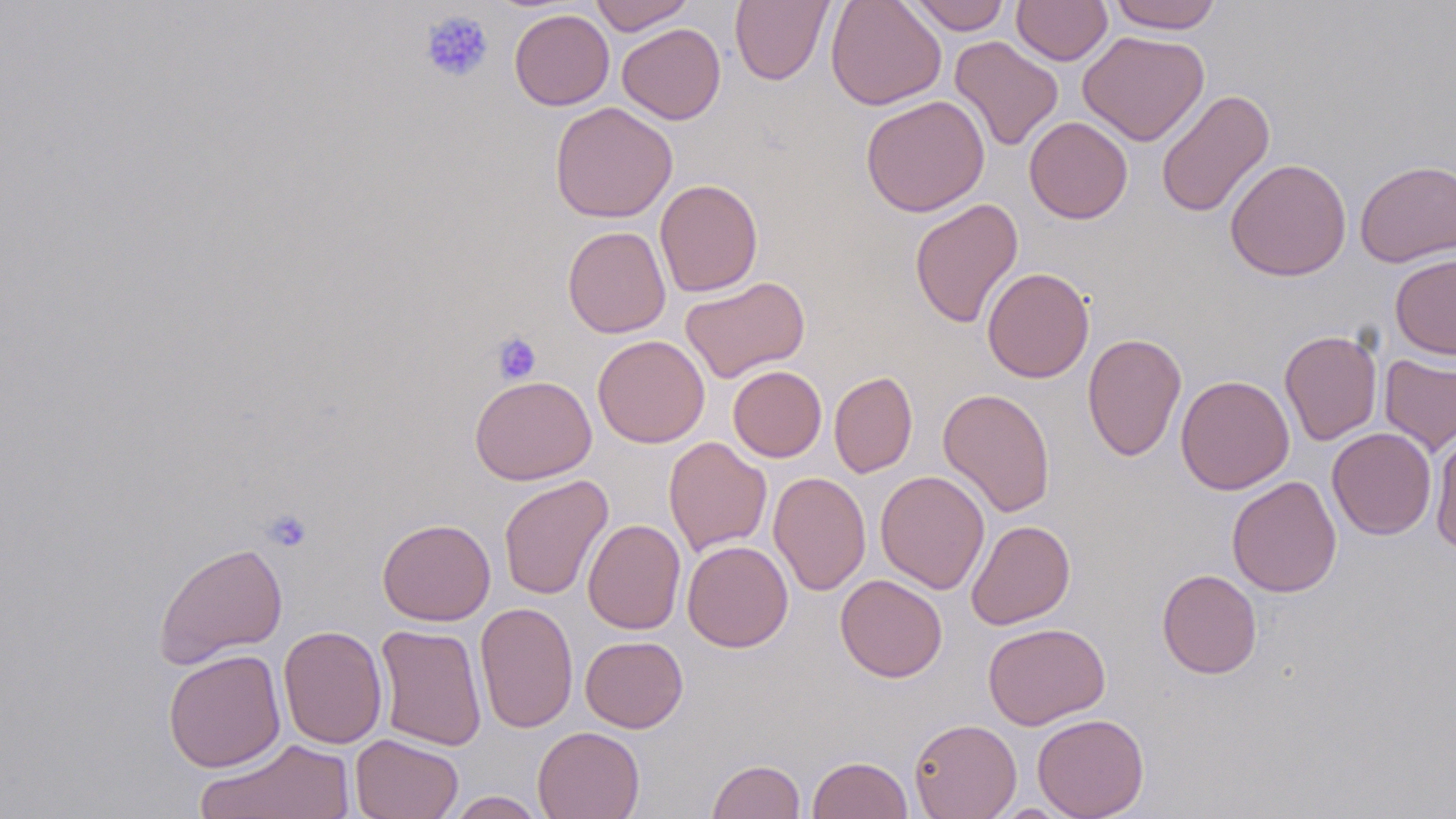

slide_level_diagnosis: no evidence of blood parasites
platelet_locations: 'approximate bounding boxes as named x1/y1/x2/y2 corners in pixels: (x1=419, y1=10, x2=494, y2=83), (x1=492, y1=331, x2=542, y2=384), (x1=263, y1=509, x2=313, y2=552)'
field_of_view: one of a larger specimen
magnification: 1000x
preparation: thin blood smear
image_size: 1456×819 pixels
stain: May-Grünwald-Giemsa
modality: light microscopy
uninfected_red_blood_cell_locations: 'approximate bounding boxes as named x1/y1/x2/y2 corners in pixels: (x1=590, y1=0, x2=694, y2=34), (x1=730, y1=0, x2=833, y2=86), (x1=826, y1=0, x2=947, y2=110), (x1=907, y1=0, x2=1010, y2=34), (x1=1011, y1=0, x2=1112, y2=66), (x1=1107, y1=0, x2=1223, y2=33), (x1=509, y1=9, x2=614, y2=110), (x1=617, y1=23, x2=726, y2=124), (x1=1078, y1=30, x2=1209, y2=146), (x1=949, y1=36, x2=1064, y2=151), (x1=1156, y1=89, x2=1275, y2=219), (x1=860, y1=95, x2=990, y2=217), (x1=549, y1=102, x2=677, y2=223), (x1=1024, y1=116, x2=1133, y2=223), (x1=1224, y1=158, x2=1352, y2=281), (x1=1355, y1=159, x2=1456, y2=267), (x1=655, y1=179, x2=763, y2=297), (x1=909, y1=198, x2=1023, y2=329), (x1=563, y1=225, x2=671, y2=338), (x1=1390, y1=253, x2=1456, y2=360), (x1=981, y1=267, x2=1094, y2=383), (x1=680, y1=276, x2=810, y2=383), (x1=1279, y1=329, x2=1382, y2=446), (x1=1082, y1=332, x2=1186, y2=462), (x1=592, y1=335, x2=710, y2=448), (x1=1379, y1=354, x2=1456, y2=457), (x1=728, y1=365, x2=827, y2=462), (x1=829, y1=370, x2=918, y2=477), (x1=469, y1=375, x2=596, y2=485), (x1=1175, y1=375, x2=1294, y2=495), (x1=937, y1=387, x2=1055, y2=518), (x1=1327, y1=427, x2=1437, y2=539), (x1=1430, y1=429, x2=1456, y2=552), (x1=664, y1=436, x2=771, y2=556), (x1=875, y1=470, x2=990, y2=594), (x1=769, y1=471, x2=871, y2=596), (x1=498, y1=475, x2=613, y2=601), (x1=1226, y1=475, x2=1342, y2=598), (x1=377, y1=518, x2=496, y2=625), (x1=583, y1=519, x2=686, y2=635), (x1=965, y1=520, x2=1076, y2=629), (x1=682, y1=540, x2=793, y2=652), (x1=153, y1=541, x2=288, y2=669), (x1=1157, y1=569, x2=1262, y2=679), (x1=835, y1=573, x2=947, y2=682), (x1=475, y1=601, x2=578, y2=733), (x1=983, y1=622, x2=1110, y2=730), (x1=374, y1=624, x2=487, y2=751), (x1=278, y1=625, x2=387, y2=749), (x1=580, y1=635, x2=688, y2=733), (x1=163, y1=649, x2=286, y2=772), (x1=1032, y1=713, x2=1149, y2=819), (x1=909, y1=718, x2=1022, y2=819), (x1=532, y1=726, x2=645, y2=819), (x1=351, y1=734, x2=463, y2=819), (x1=195, y1=739, x2=357, y2=819), (x1=807, y1=755, x2=914, y2=818), (x1=707, y1=759, x2=805, y2=819), (x1=444, y1=790, x2=548, y2=818)'